Locate every Plasmodium parasite.
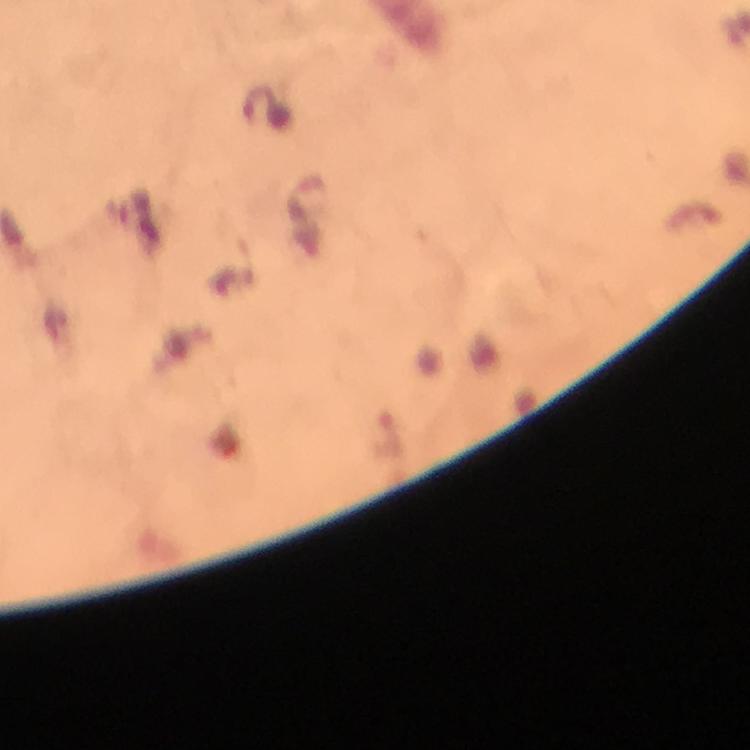

Approximate object centers, in pixels from the top-left corner.
Plasmodium parasites: (x=265, y=109).

image size = 750×750 pixels
immersion oil = applied
stain = Giemsa
preparation = thick smear
cropped from = one field of view
capture = smartphone camera through the microscope
context = from a malaria diagnostic workup
magnification = 100x